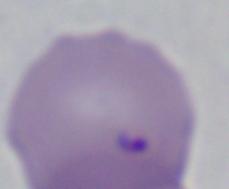
A Babesia parasite is shown. Photomicrograph. Captured at 1000x magnification.